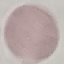
malaria status = uninfected
image type = cell patch, automatically extracted from a larger field of view and resized to 64 × 64 pixels
preparation = thin blood smear
capture = smartphone through the microscope eyepiece
stain = Giemsa